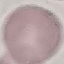
Summary:
  - Result: negative for malaria parasites
  - Image type: cell patch, automatically extracted from a larger field of view and resized to 64 × 64 pixels
  - Preparation: thin blood smear
  - Capture: smartphone camera at the microscope eyepiece
  - Stain: Giemsa